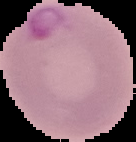
result = malaria parasites detected
image size = 136×142 pixels
preparation = thin blood film
image type = segmented cell region on a black background